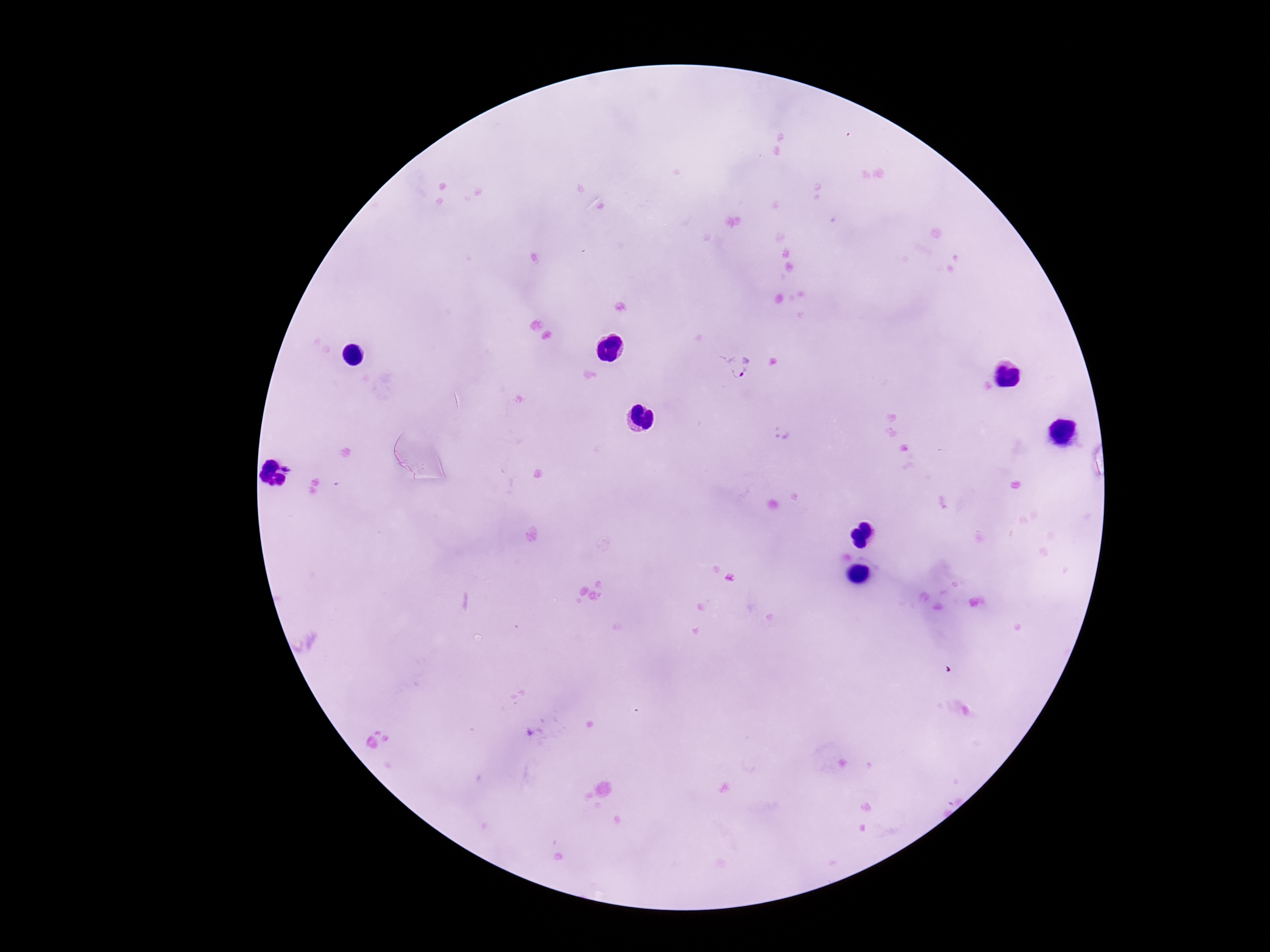
Approximate centers as {x, y} in pixels.
Summary:
  - Plasmodium parasite locations: {738, 365}
  - Magnification: 100x
  - Capture: smartphone camera through the microscope eyepiece
  - Image size: 1270×952 pixels
  - Field of view: one from this slide
  - Stain: Giemsa
  - Patient malaria status: infected
  - Preparation: thick blood smear